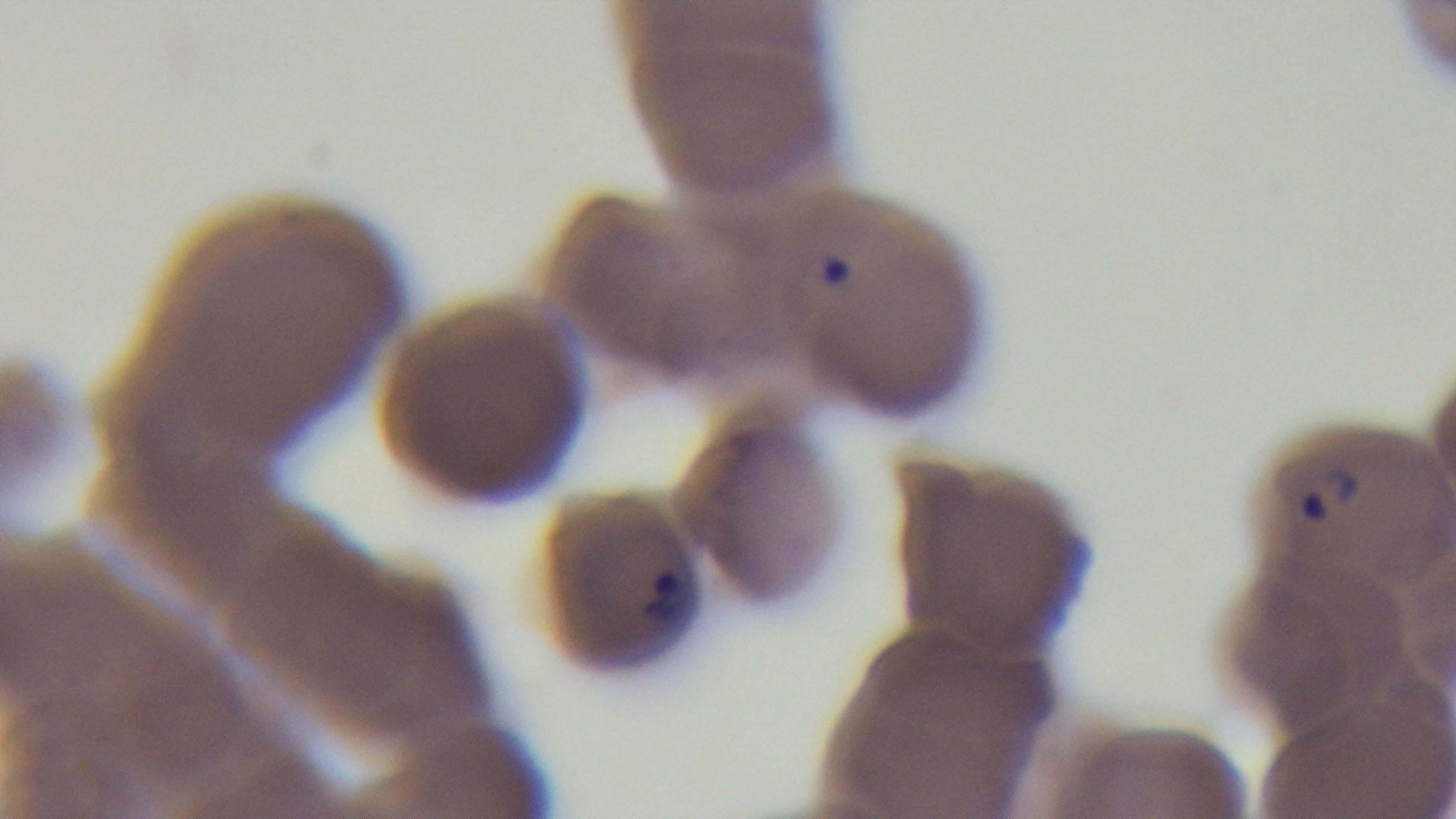 Photomicrograph. Preparation: thin smear. Malaria status: infected. Mounted 4K digital camera. One field from the slide. Giemsa-stained. Oil-immersion objective, 100x.